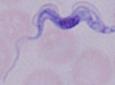 1000x magnification. A trypanosome is seen. Photomicrograph.